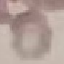
Malaria status: uninfected. Thin smear of blood. Giemsa stain. Photographed with a smartphone camera at the microscope eyepiece. Cell patch, automatically extracted from a larger field of view and resized to 64 × 64 pixels.